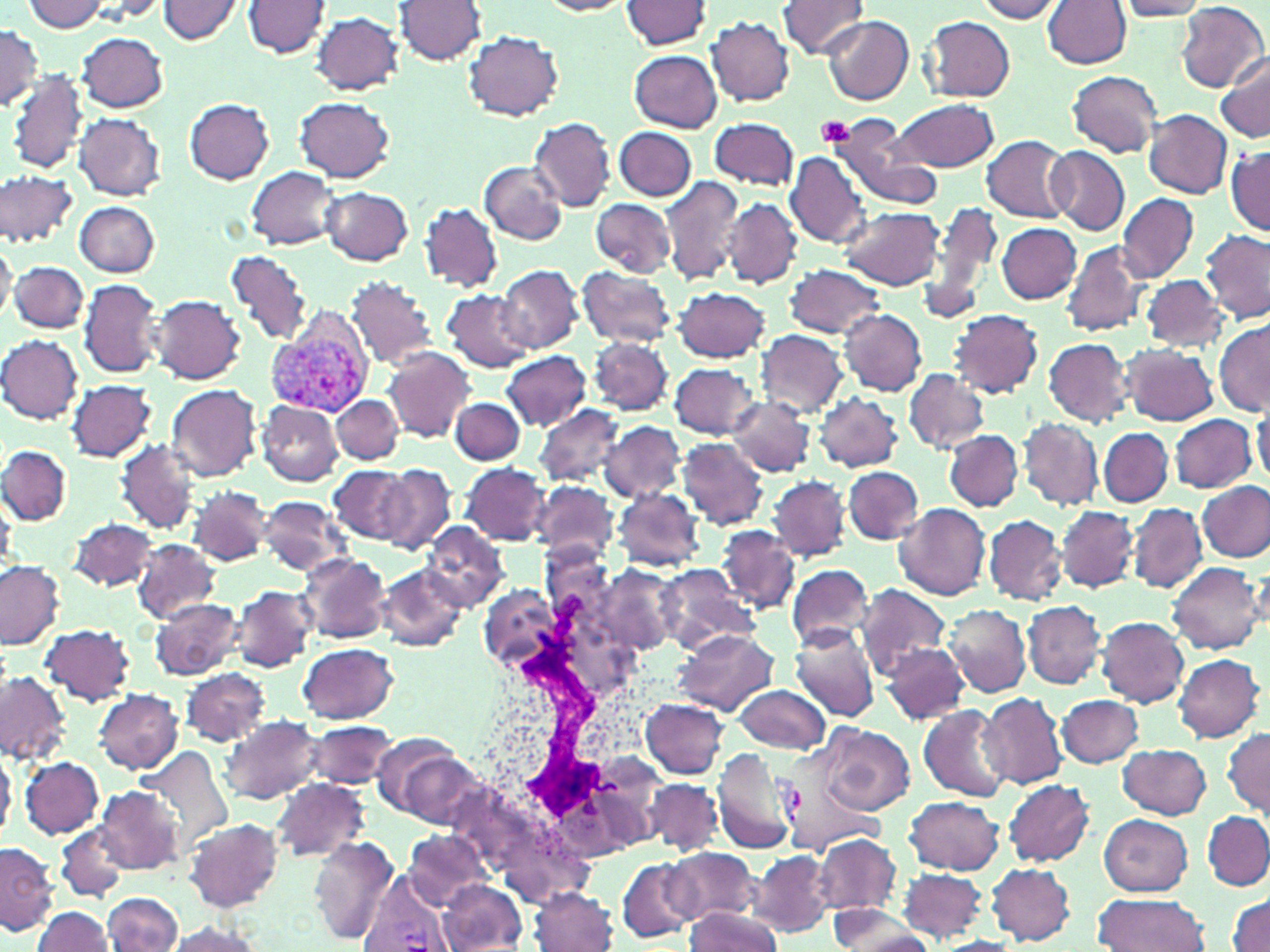
Summary:
  - Coordinate format: approximate bounding boxes as (x1,y1)-(x2,y2) corner pairs in pixels
  - Uninfected red blood cell locations: (156,0)-(244,44), (243,0)-(330,60), (394,0)-(486,66), (536,0)-(632,17), (975,0)-(1065,22), (25,1)-(109,33), (622,1)-(712,48), (777,1)-(869,58), (1043,1)-(1129,69), (1113,1)-(1213,22), (1177,3)-(1268,90), (309,8)-(488,80), (311,11)-(404,95), (821,15)-(913,105), (707,16)-(795,105), (922,16)-(1016,101), (0,25)-(42,111), (464,30)-(564,120), (77,33)-(168,112), (630,50)-(723,131), (1219,53)-(1270,142), (7,70)-(87,175), (1067,70)-(1163,157), (184,97)-(275,183), (296,97)-(395,180), (891,98)-(1000,172), (1143,109)-(1231,198), (74,112)-(166,201), (710,117)-(800,190), (832,117)-(943,211), (530,118)-(617,212), (614,126)-(697,200), (982,135)-(1074,222), (1045,146)-(1129,237), (1227,147)-(1269,236), (786,151)-(871,247), (478,160)-(567,245), (246,166)-(341,248), (0,169)-(77,248), (661,174)-(746,286), (322,187)-(413,265), (1116,192)-(1199,281), (591,198)-(675,275), (723,198)-(802,289), (74,201)-(160,276), (923,202)-(1004,320), (420,203)-(501,291), (838,206)-(945,290), (997,222)-(1083,304), (1201,229)-(1270,324), (0,237)-(17,323), (1061,240)-(1148,337), (225,248)-(313,345), (11,260)-(87,333), (784,262)-(889,340), (498,265)-(582,352), (576,266)-(677,347), (1140,275)-(1227,353), (344,276)-(438,368), (80,277)-(164,378), (672,287)-(771,363), (442,290)-(533,371), (150,295)-(246,384), (838,309)-(927,396), (949,309)-(1043,397), (1214,321)-(1270,416), (755,329)-(847,417), (0,335)-(83,422), (589,336)-(673,414), (1043,337)-(1133,426), (1123,345)-(1218,425), (383,347)-(476,441), (501,350)-(593,431), (669,362)-(759,438), (902,369)-(989,455), (66,379)-(156,461), (166,383)-(261,482), (816,392)-(903,471), (826,392)-(909,544), (727,395)-(815,477), (332,396)-(402,465), (449,397)-(526,466), (257,401)-(342,485), (535,403)-(625,487), (1252,406)-(1269,487), (1169,413)-(1257,493), (1019,417)-(1103,511), (1187,418)-(1262,560), (598,420)-(688,503), (1099,427)-(1173,507), (945,429)-(1023,511), (117,438)-(201,534), (678,439)-(767,530), (1,445)-(72,524), (461,462)-(550,544), (377,464)-(455,554), (331,466)-(413,545), (844,467)-(923,544), (767,474)-(849,561), (530,481)-(620,561), (1197,482)-(1269,562), (189,487)-(271,564), (614,487)-(705,570), (1,491)-(16,573), (255,497)-(352,577), (894,502)-(991,600), (1128,502)-(1206,594), (1056,505)-(1137,591), (984,515)-(1067,606), (69,518)-(157,590), (419,523)-(508,610), (719,526)-(799,612), (131,539)-(221,623), (297,553)-(390,643), (0,562)-(65,650), (1168,562)-(1265,656), (373,563)-(468,652), (786,563)-(875,651), (596,564)-(681,658), (653,565)-(754,651), (856,584)-(950,679), (231,585)-(316,674), (479,585)-(564,672), (149,599)-(244,681), (1022,600)-(1105,690), (943,604)-(1032,695), (1097,616)-(1189,706), (42,624)-(134,705), (674,628)-(779,716), (789,629)-(880,724), (298,642)-(399,723), (881,642)-(969,724), (1172,654)-(1264,743), (180,667)-(272,747), (0,672)-(69,764), (733,684)-(830,753), (92,689)-(183,773), (980,693)-(1068,788), (1056,694)-(1144,767), (641,699)-(729,778), (921,706)-(1012,801), (221,715)-(323,806), (776,717)-(880,858), (305,721)-(398,791), (819,724)-(915,815), (1223,727)-(1269,813), (378,738)-(480,826), (1119,743)-(1211,819), (142,746)-(233,852), (0,749)-(18,835), (20,758)-(104,837), (270,777)-(370,863), (646,779)-(721,855), (1002,779)-(1096,867), (94,784)-(185,874), (904,796)-(1005,874), (1203,812)-(1269,890), (1099,814)-(1193,896), (184,818)-(283,911), (55,825)-(128,902), (402,830)-(492,909), (310,834)-(398,946), (815,834)-(900,916), (0,841)-(58,934), (666,849)-(758,924), (749,850)-(834,937), (617,857)-(697,943), (987,863)-(1075,944), (899,869)-(987,940), (437,880)-(527,951), (530,887)-(619,952), (103,893)-(181,951), (1093,893)-(1209,951), (1229,895)-(1269,951), (828,905)-(931,951), (31,907)-(114,952), (682,908)-(783,952), (163,921)-(267,952), (936,937)-(1023,951)
  - White blood cell locations: (479,587)-(688,834)
  - Platelet locations: (818,117)-(856,148)
  - Plasmodium vivax-infected red blood cell locations: (267,307)-(378,420), (711,748)-(809,856), (361,873)-(452,952)
  - Slide-level diagnosis: Plasmodium vivax
  - Modality: light microscopy
  - Preparation: thin blood smear
  - Magnification: 1000x
  - Image size: 1270×952 pixels
  - Stain: May-Grünwald-Giemsa
  - Field of view: one of a larger specimen